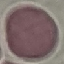 Malaria status: uninfected. Thin smear of blood. Automatically extracted cell patch, resized to 64 × 64 pixels. Giemsa stain. Photographed with a smartphone camera at the microscope eyepiece.